Classify this cell by malaria status.
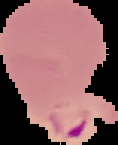

Parasitized.

image_type: segmented cell region with the area outside set to black
image_size: 118×145 pixels
preparation: thin blood film